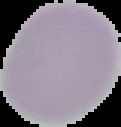

malaria status = uninfected
image size = 121×127 pixels
preparation = thin blood film
image type = segmented cell region with the area outside set to black